Report the malaria status of this cell.
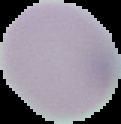

It is uninfected.

From a thin blood film. The area outside the segmented cell region is set to black. Image is 121×124 pixels.